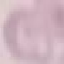
Summary:
  - Result: negative for malaria parasites
  - Stain: Giemsa
  - Capture: smartphone camera at the microscope eyepiece
  - Image type: automatically extracted cell patch, resized to 64 × 64 pixels
  - Preparation: thin blood smear